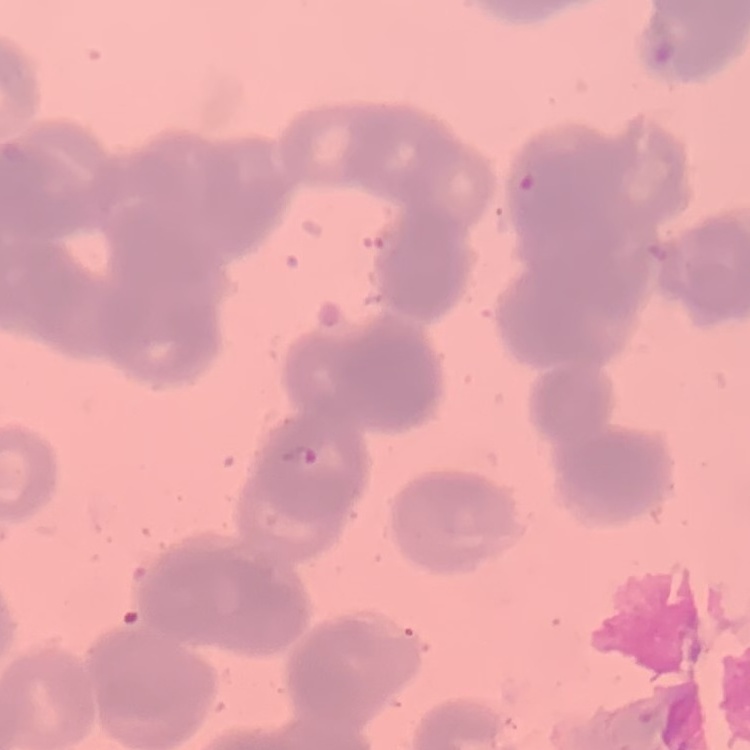

Summary:
  - Red blood cell morphology: rouleaux formation
  - Preparation: thin blood smear
  - Image type: one tile cut from a larger photomicrograph
  - Stain: Field's or Giemsa